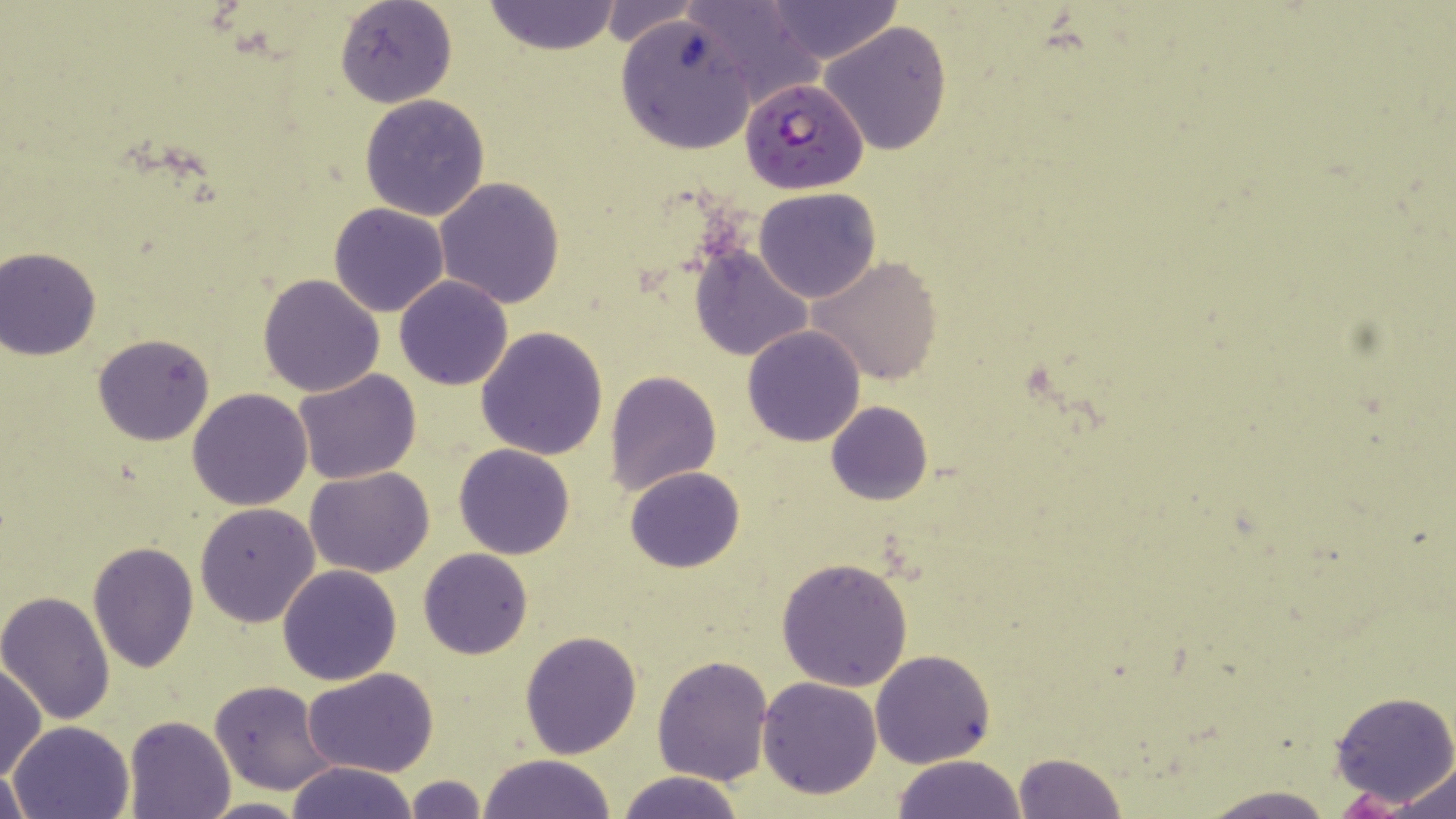
Plasmodium falciparum-infected red blood cell locations = approximate bounding boxes as named x1/y1/x2/y2 corners in pixels: (x1=738, y1=76, x2=868, y2=194)
slide-level diagnosis = Plasmodium falciparum
uninfected red blood cell locations = approximate bounding boxes as named x1/y1/x2/y2 corners in pixels: (x1=334, y1=0, x2=456, y2=109), (x1=685, y1=0, x2=823, y2=108), (x1=760, y1=0, x2=903, y2=63), (x1=600, y1=1, x2=701, y2=49), (x1=483, y1=2, x2=621, y2=55), (x1=615, y1=14, x2=757, y2=155), (x1=819, y1=20, x2=953, y2=156), (x1=359, y1=94, x2=490, y2=222), (x1=434, y1=176, x2=565, y2=308), (x1=755, y1=187, x2=881, y2=304), (x1=329, y1=202, x2=448, y2=317), (x1=690, y1=245, x2=814, y2=361), (x1=0, y1=247, x2=102, y2=359), (x1=809, y1=255, x2=943, y2=386), (x1=258, y1=273, x2=385, y2=397), (x1=394, y1=277, x2=512, y2=391), (x1=741, y1=326, x2=867, y2=447), (x1=476, y1=327, x2=607, y2=462), (x1=92, y1=333, x2=216, y2=445), (x1=293, y1=368, x2=422, y2=485), (x1=605, y1=370, x2=721, y2=494), (x1=188, y1=389, x2=313, y2=511), (x1=825, y1=400, x2=933, y2=506), (x1=453, y1=444, x2=575, y2=560), (x1=625, y1=466, x2=745, y2=575), (x1=307, y1=467, x2=435, y2=578), (x1=195, y1=502, x2=320, y2=628), (x1=87, y1=541, x2=199, y2=672), (x1=418, y1=548, x2=533, y2=660), (x1=775, y1=555, x2=914, y2=691), (x1=277, y1=563, x2=402, y2=685), (x1=1, y1=590, x2=118, y2=725), (x1=519, y1=630, x2=642, y2=759), (x1=870, y1=649, x2=997, y2=768), (x1=651, y1=655, x2=774, y2=788), (x1=0, y1=663, x2=46, y2=781), (x1=303, y1=668, x2=441, y2=780), (x1=757, y1=676, x2=882, y2=799), (x1=208, y1=679, x2=339, y2=795), (x1=1329, y1=689, x2=1456, y2=810), (x1=123, y1=716, x2=235, y2=819), (x1=7, y1=720, x2=135, y2=819), (x1=1012, y1=749, x2=1127, y2=819), (x1=478, y1=754, x2=616, y2=819), (x1=891, y1=755, x2=1028, y2=819), (x1=285, y1=761, x2=419, y2=819), (x1=1388, y1=762, x2=1456, y2=817), (x1=0, y1=765, x2=31, y2=818), (x1=613, y1=771, x2=749, y2=819), (x1=404, y1=774, x2=487, y2=818), (x1=1194, y1=783, x2=1337, y2=818), (x1=196, y1=797, x2=312, y2=817)
magnification = 1000x
modality = optical microscopy
preparation = thin blood smear
image size = 1456×819 pixels
stain = May-Grünwald-Giemsa
field of view = one of a larger specimen